State which parasite is depicted.
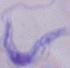
This is a trypanosome.

1000x magnification. Micrograph.